Name the parasite shown.
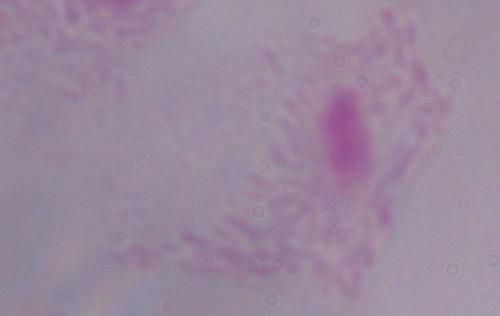
This is a trichomonad.

magnification: 1000x
modality: micrograph